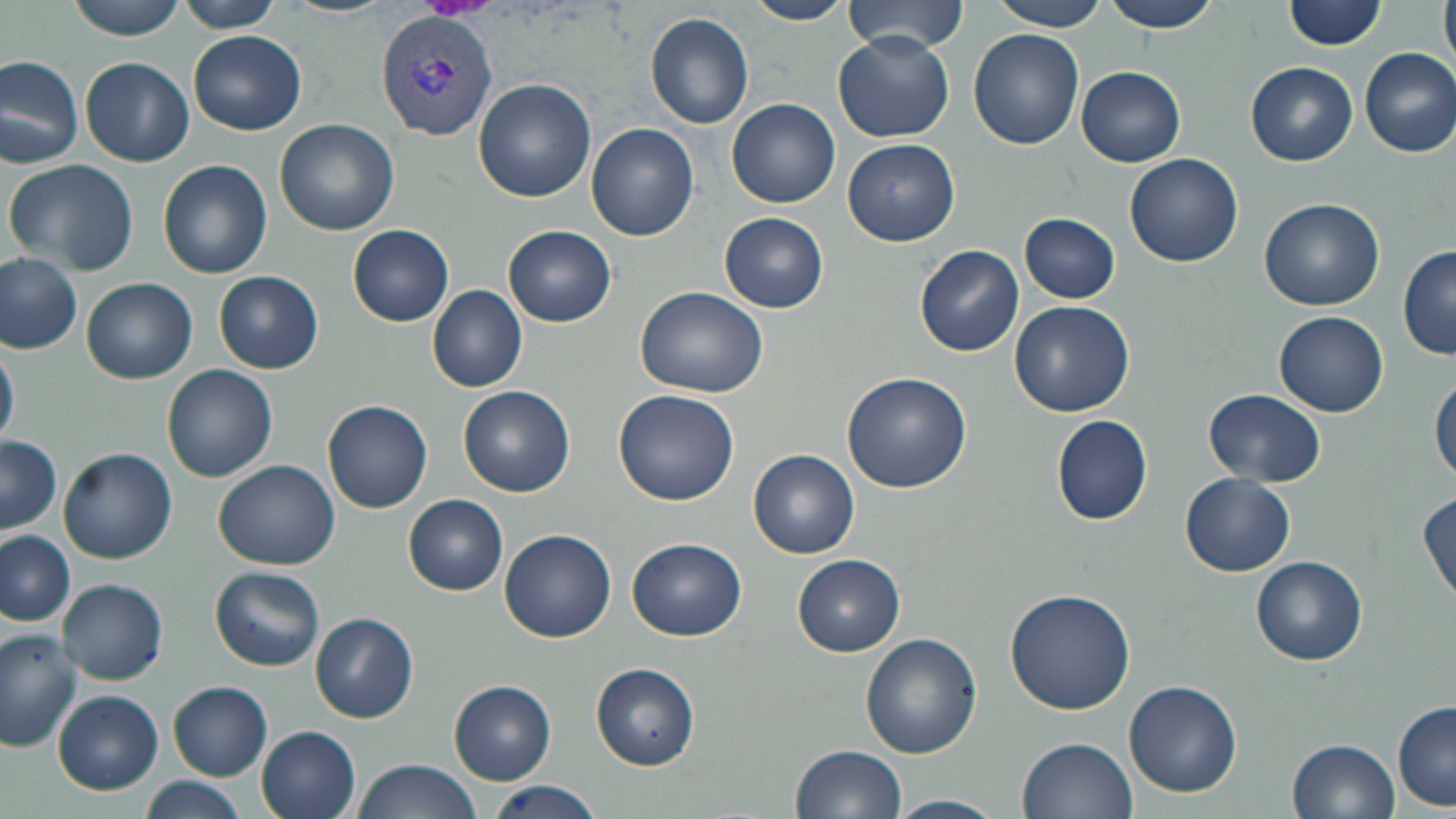
Approximate bounding boxes as (x1,y1)-(x2,y2) corner pairs in pixels. Uninfected red blood cell locations: (64,0)-(190,39), (178,0)-(291,32), (284,0)-(393,18), (746,0)-(853,24), (844,0)-(968,53), (986,0)-(1112,30), (1098,0)-(1224,31), (1285,0)-(1386,50), (1439,0)-(1455,72), (646,12)-(755,128), (969,29)-(1084,149), (189,30)-(306,135), (834,32)-(954,142), (1359,49)-(1456,156), (0,52)-(85,169), (80,57)-(194,166), (1246,62)-(1358,165), (1077,66)-(1186,166), (474,80)-(597,203), (727,99)-(840,209), (275,119)-(400,235), (587,124)-(700,241), (843,139)-(961,247), (1125,153)-(1243,267), (5,157)-(141,277), (157,159)-(272,278), (1260,197)-(1383,309), (719,212)-(829,312), (1019,213)-(1121,303), (347,223)-(454,327), (504,224)-(617,327), (916,245)-(1025,357), (1399,247)-(1456,360), (0,253)-(82,355), (214,271)-(324,374), (81,278)-(197,384), (427,286)-(528,393), (635,286)-(768,398), (1010,300)-(1134,417), (1274,311)-(1388,416), (0,341)-(18,449), (162,363)-(278,481), (842,372)-(972,494), (1431,373)-(1455,484), (458,385)-(575,497), (614,389)-(739,505), (1204,389)-(1326,486), (322,399)-(433,514), (1051,414)-(1153,525), (1,436)-(61,535), (59,448)-(177,564), (749,449)-(860,559), (213,460)-(340,569), (1180,474)-(1295,577), (1418,491)-(1454,604), (403,494)-(509,595), (498,529)-(616,642), (0,531)-(77,627), (627,538)-(747,640), (792,553)-(904,655), (1252,555)-(1369,665), (210,566)-(326,670), (58,578)-(168,685), (1004,587)-(1134,717), (309,612)-(419,724), (0,628)-(85,751), (860,632)-(981,758), (590,662)-(699,769), (1125,680)-(1242,797), (168,681)-(273,780), (450,681)-(556,784), (52,689)-(162,793), (1391,701)-(1455,811), (257,726)-(361,819), (1018,736)-(1137,818), (1289,737)-(1401,819), (790,744)-(907,819), (351,759)-(480,819), (139,777)-(247,819), (486,778)-(605,819), (888,795)-(1004,819). Plasmodium vivax-infected red blood cell locations: (375,9)-(498,142). Slide-level diagnosis: Plasmodium vivax. 1000x magnification. May-Grünwald-Giemsa stain. Thin blood film. Light microscopy. Image is 1456×819 pixels. Single field of view.